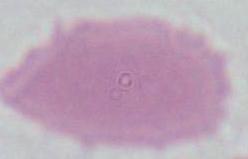

identification = erythrocyte
magnification = 1000x
modality = photomicrograph